Give the position of every malaria parasite.
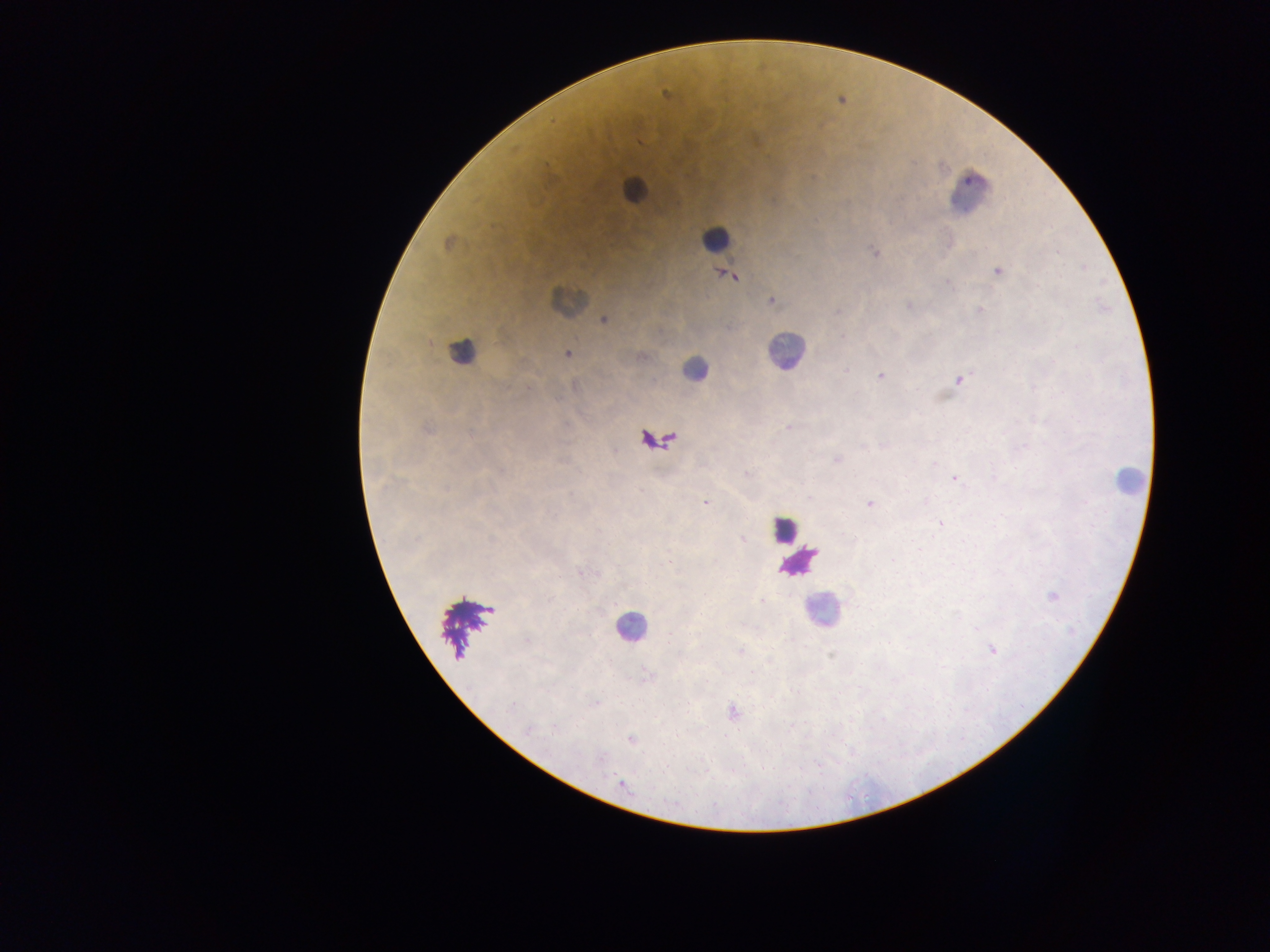
Approximate centers as (x, y) in pixels.
Malaria parasites: (667, 96), (641, 141), (448, 243), (874, 252), (1058, 252), (1085, 268), (997, 271), (730, 276), (949, 284), (1038, 285), (771, 301), (908, 305), (979, 310), (604, 320), (567, 354), (641, 357), (846, 370), (881, 376), (959, 380), (788, 428), (426, 429), (862, 445), (885, 445), (1025, 446), (836, 459), (746, 474), (955, 479), (705, 503), (869, 504), (939, 523), (742, 540), (579, 572), (1052, 596), (762, 601), (527, 641), (740, 651), (992, 651), (649, 675), (595, 703), (511, 707), (734, 712), (528, 730), (631, 740), (601, 759), (623, 785).

capture = mobile-phone photograph through a microscope
image size = 1270×952 pixels
country = Ghana
leukocyte locations = approximate centers as (x, y) in pixels: (633, 190), (970, 193), (715, 237), (567, 300), (461, 351), (785, 351), (694, 369), (1128, 479), (783, 529), (798, 562), (822, 610), (631, 627)
preparation = thick blood film
field of view = single